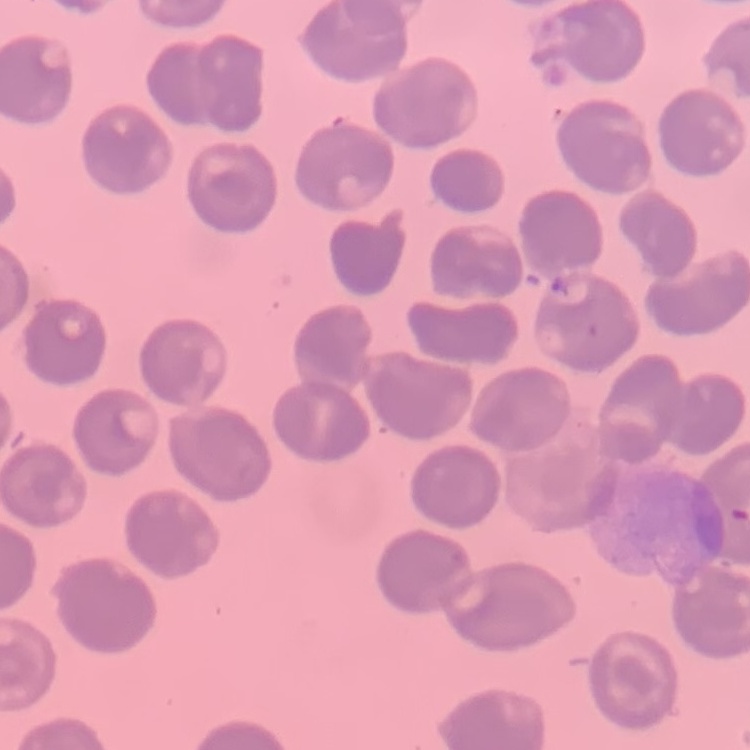
Summary:
  - Red blood cell morphology: no rouleaux formation
  - Stain: Field's or Giemsa
  - Preparation: thin blood film
  - Image type: one tile cut from a larger photomicrograph